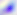

{
  "magnification": "400x",
  "identification": "Toxoplasma gondii",
  "modality": "micrograph"
}